Assess for Plasmodium parasites.
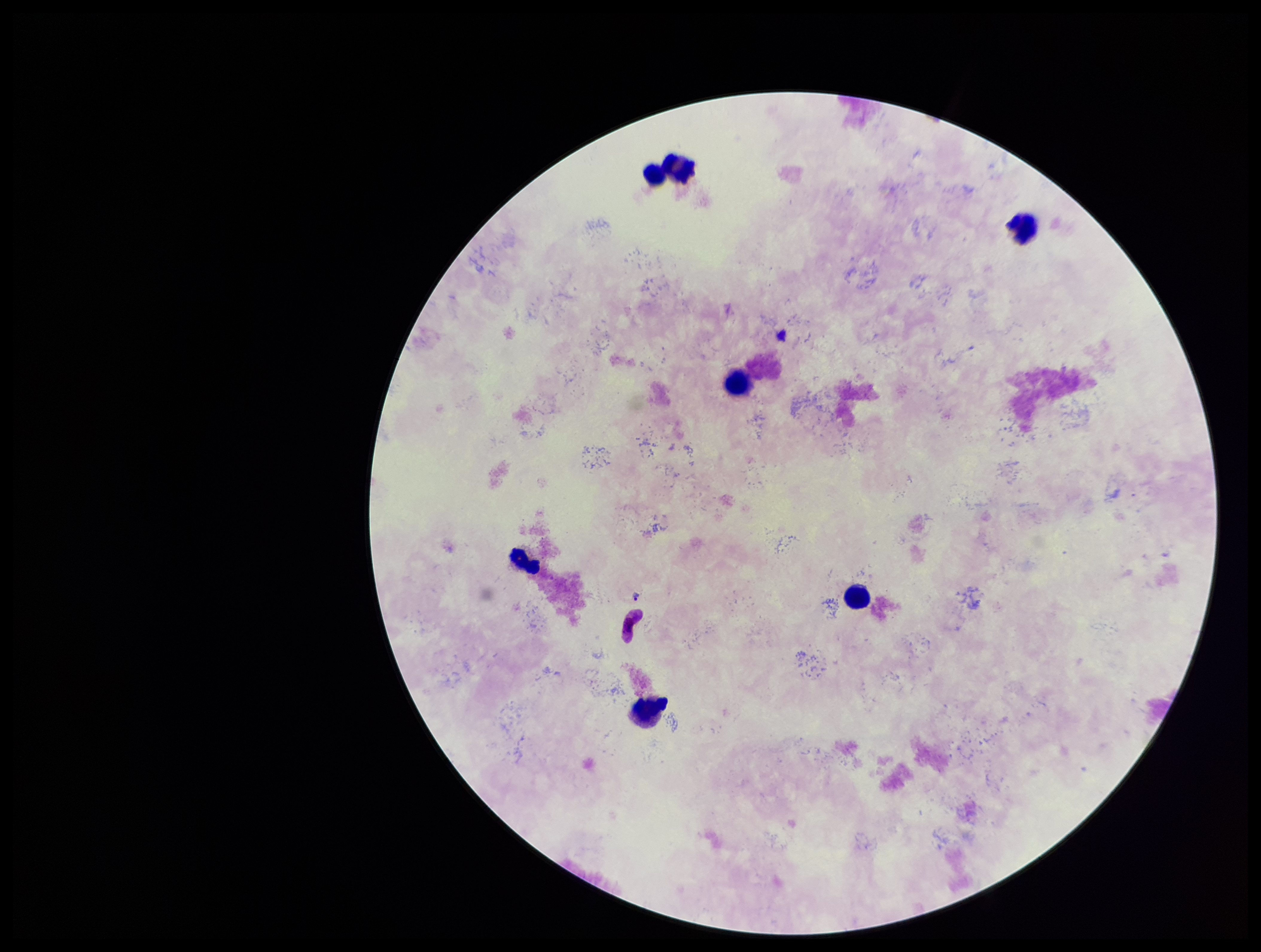

Identified.

Photographed through the microscope eyepiece with a smartphone camera. Species reported for this patient: Plasmodium falciparum. Preparation: thick smear. Parasite count: 1. Image is 1261×952 pixels. Giemsa stain. Leukocyte count: 7. Patient malaria status: infected. One field from this slide.